Report the malaria status of this cell.
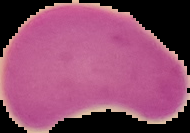

It is uninfected.

Summary:
  - Image type: segmented cell region on a black background
  - Image size: 190×133 pixels
  - Preparation: thin blood film